Locate every Plasmodium parasite.
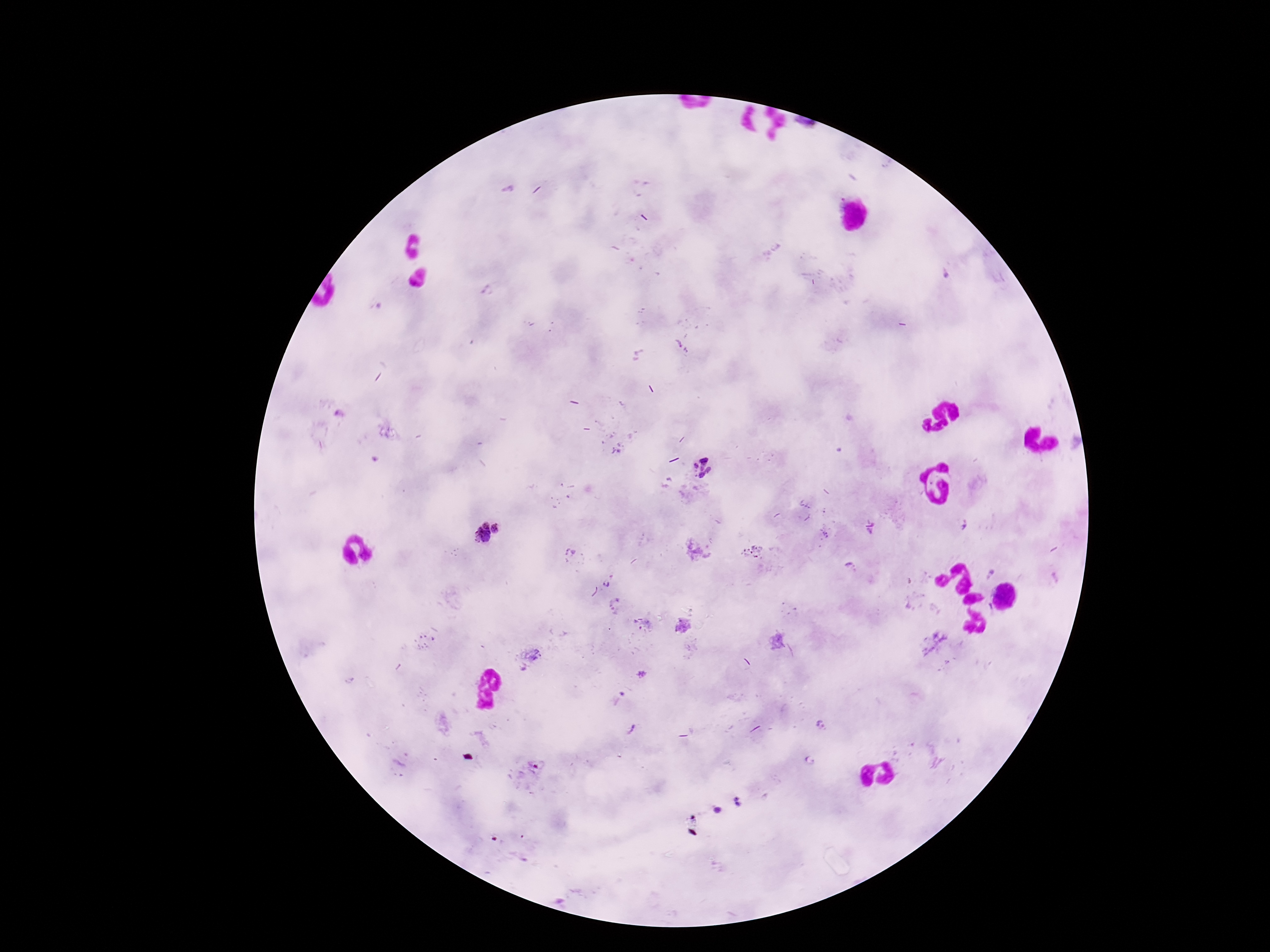
Approximate object centers, in pixels from the top-left corner.
Plasmodium parasites: (x=703, y=463), (x=695, y=466), (x=710, y=470), (x=702, y=475), (x=487, y=524), (x=497, y=529), (x=482, y=537), (x=607, y=583), (x=822, y=725), (x=809, y=760).

Summary:
  - Patient malaria status: positive
  - Magnification: 100x
  - Image size: 1270×952 pixels
  - Stain: Giemsa
  - Preparation: thick blood film
  - Field of view: one from this slide
  - Capture: smartphone camera through the microscope eyepiece